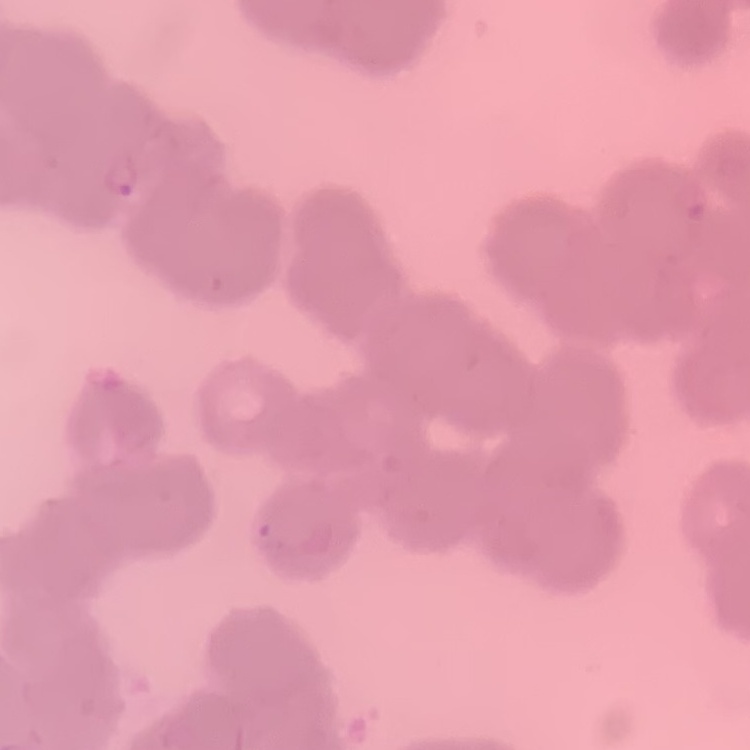
The red blood cells show rouleaux formation. One tile cut from a larger photomicrograph. Stained with either Field's or Giemsa. Thin blood smear.